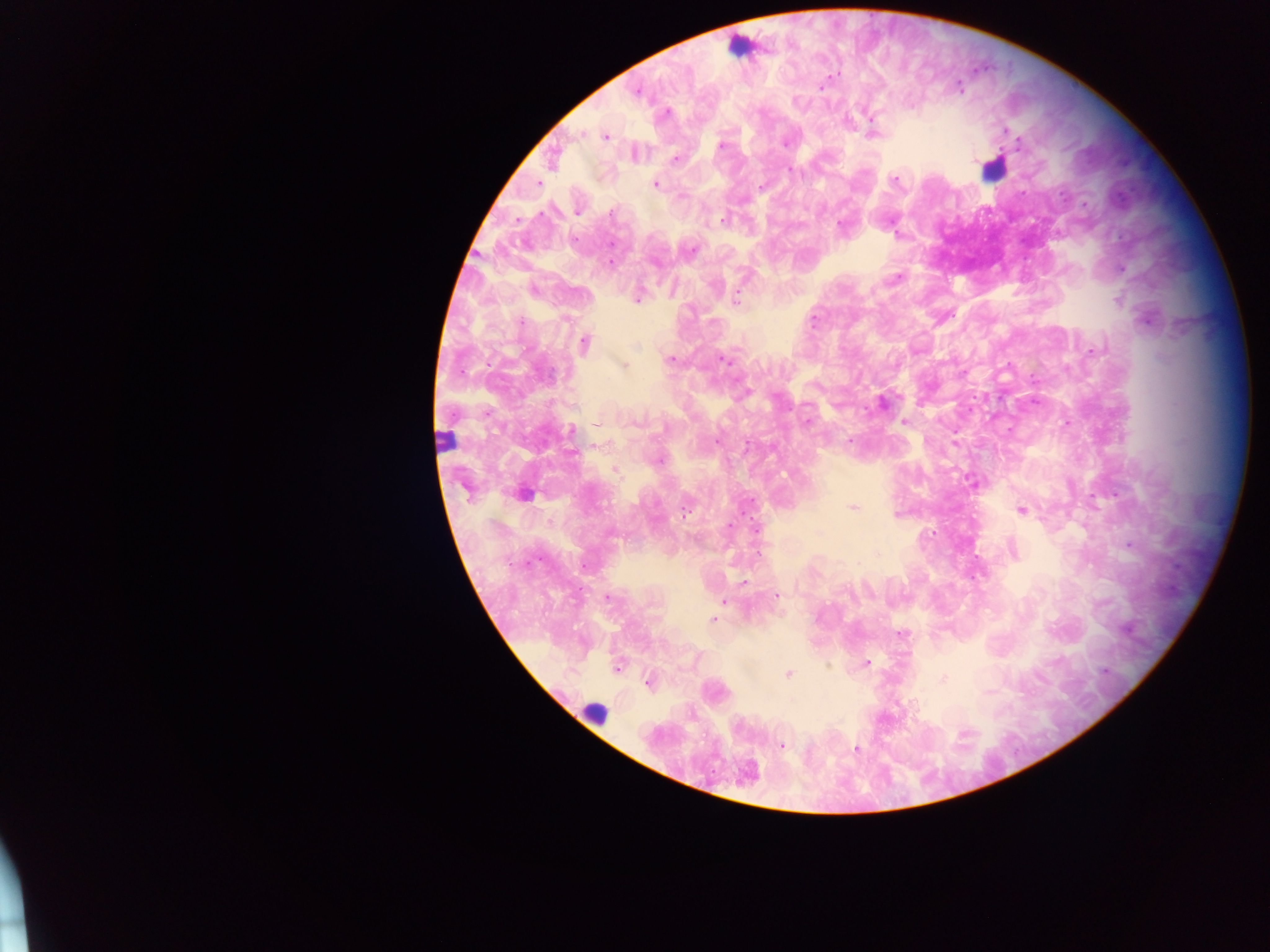
capture = mobile-phone photograph through a microscope
leukocyte locations = approximate centers as x y in pixels: 741 43; 993 169; 444 442; 523 492; 594 714
country = Ghana
malaria parasite locations = approximate centers as x y in pixels: 960 86; 821 87; 637 92; 666 113; 871 121; 1006 130; 581 134; 873 134; 605 136; 785 144; 1017 145; 721 146; 676 158; 789 171; 895 180; 538 183; 655 184; 760 187; 1023 192; 577 210; 611 214; 722 220; 841 225; 898 235; 574 239; 691 250; 611 262; 1122 269; 896 278; 1117 300; 636 301; 736 301; 522 321; 1146 321; 813 322; 585 342; 636 348; 1093 351; 671 359; 723 359; 623 365; 962 373; 882 402; 904 421; 808 422; 597 424; 571 431; 850 440; 716 442; 954 444; 659 461; 615 470; 971 482; 853 507; 1021 510; 685 511; 896 514; 729 526; 757 529; 1129 546; 744 582; 777 595; 607 597; 725 601; 713 620; 902 634; 866 663; 617 667; 1105 671; 788 674; 943 680; 648 683; 782 746; 857 749
field of view = single
image size = 1270×952 pixels
preparation = thick blood smear